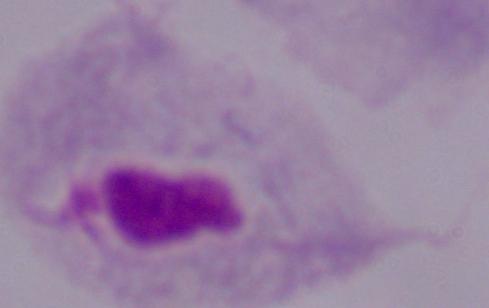
Summary:
  - Identification: trichomonad
  - Magnification: 1000x
  - Modality: micrograph